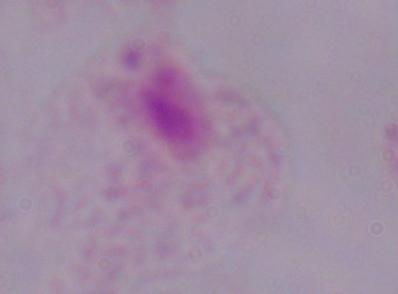
{
  "modality": "photomicrograph",
  "identification": "trichomonad",
  "magnification": "1000x"
}